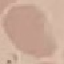
Summary:
  - Malaria status: uninfected
  - Preparation: thin smear
  - Stain: Giemsa
  - Image type: automatically extracted cell patch, resized to 64 × 64 pixels
  - Capture: smartphone camera at the microscope eyepiece